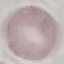

Malaria status: uninfected. Photographed with a smartphone camera at the microscope eyepiece. Cell patch, automatically extracted from a larger field of view and resized to 64 × 64 pixels. Thin smear of blood. Giemsa stain.